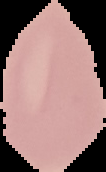 From a thin blood smear. Malaria status: uninfected. Segmented cell region on a black background. Image is 106×172 pixels.